Locate every Plasmodium parasite.
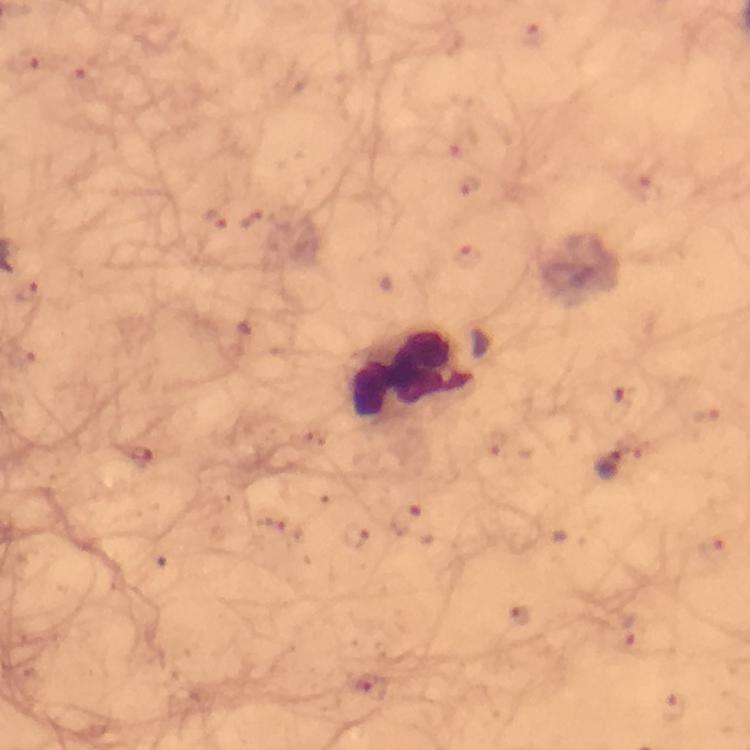
Approximate centers as {x, y} in pixels.
Plasmodium parasites: {535, 36}, {214, 219}, {469, 257}, {623, 396}, {610, 465}, {714, 548}, {522, 618}, {629, 629}, {370, 688}, {675, 705}.

Summary:
  - Leukocyte locations: {413, 375}
  - Preparation: thick blood smear
  - Magnification: 100x
  - Context: from a malaria diagnostic workup
  - Cropped from: one field of view
  - Image size: 750×750 pixels
  - Stain: Giemsa
  - Capture: smartphone camera through the microscope
  - Immersion oil: used